Report the malaria status of this cell.
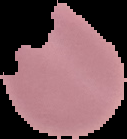

Parasitized.

From a thin blood film. Image is 127×139 pixels. Cell region segmented out of the field of view; the surrounding area is masked to black.